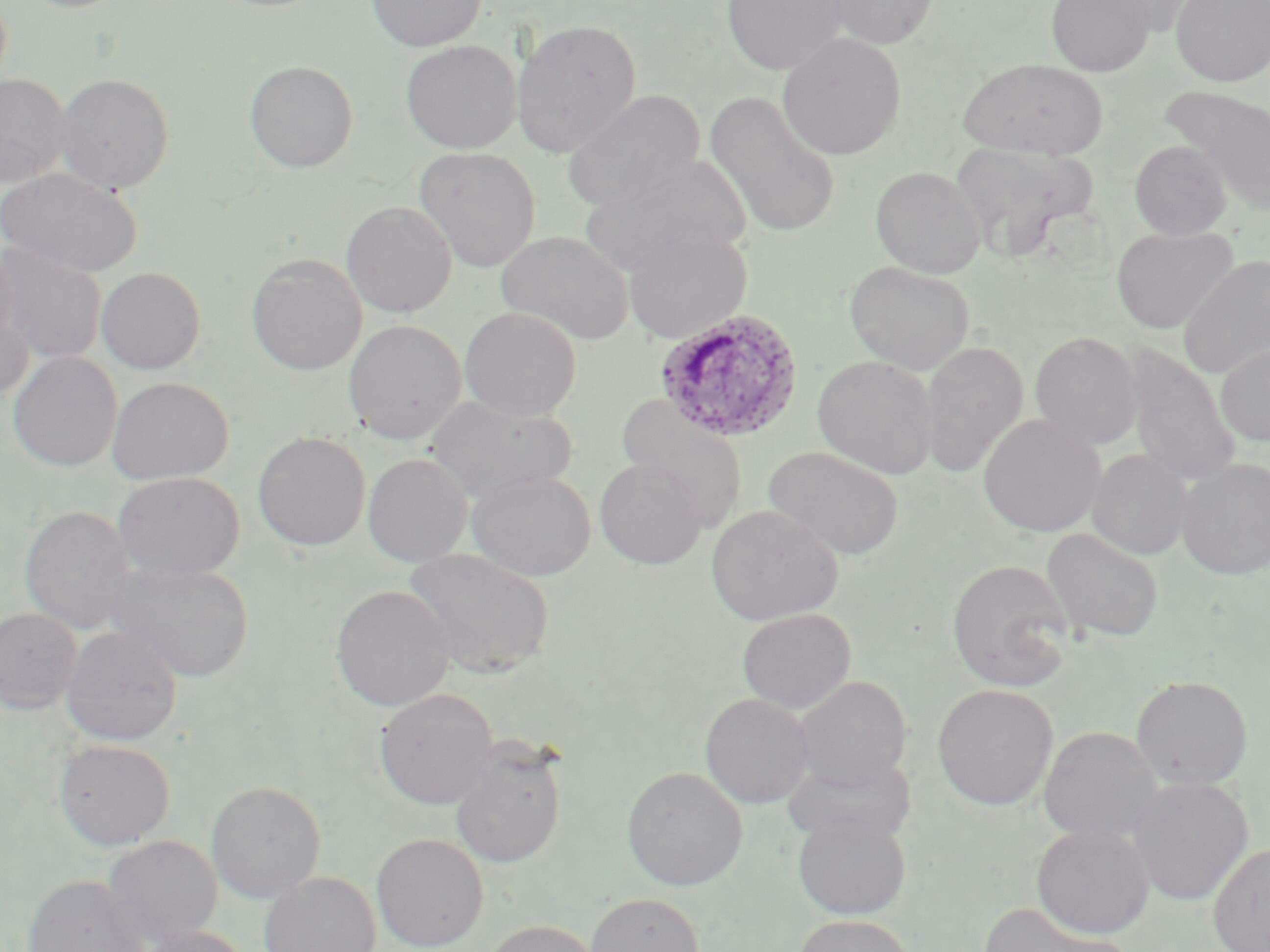
Summary:
  - Coordinate format: approximate bounding boxes as (x1,y1)-(x2,y2) corner pairs in pixels
  - Plasmodium ovale-infected red blood cell locations: (654,309)-(804,444)
  - Uninfected red blood cell locations: (366,0)-(486,52), (721,0)-(849,74), (822,0)-(939,50), (1046,0)-(1156,76), (1170,1)-(1270,87), (510,19)-(642,157), (776,33)-(907,161), (400,40)-(522,153), (959,57)-(1109,159), (244,60)-(358,172), (54,73)-(174,193), (0,74)-(71,188), (1162,86)-(1270,215), (562,89)-(706,212), (705,91)-(842,239), (1129,139)-(1232,239), (950,141)-(1096,261), (414,147)-(541,273), (580,155)-(752,276), (870,166)-(986,278), (0,167)-(142,276), (340,200)-(457,317), (622,224)-(752,344), (1111,226)-(1238,334), (495,230)-(635,344), (0,240)-(21,351), (1,243)-(107,365), (246,253)-(367,375), (1178,255)-(1270,378), (845,261)-(976,375), (96,266)-(206,373), (0,303)-(34,407), (459,307)-(582,421), (343,319)-(466,445), (1030,331)-(1143,448), (919,340)-(1029,479), (1215,342)-(1270,447), (1123,346)-(1241,482), (8,351)-(122,471), (812,355)-(940,479), (107,376)-(233,484), (425,394)-(576,503), (617,395)-(750,532), (978,413)-(1106,538), (252,431)-(371,551), (764,446)-(905,560), (1085,449)-(1195,560), (363,452)-(472,567), (595,457)-(709,569), (1175,458)-(1270,580), (465,468)-(596,582), (112,471)-(244,583), (706,504)-(843,626), (19,505)-(136,635), (1042,527)-(1165,643), (403,547)-(555,680), (946,558)-(1076,691), (103,561)-(255,682), (330,584)-(455,712), (0,607)-(82,713), (736,608)-(856,714), (61,625)-(182,745), (793,674)-(912,791), (1130,675)-(1254,791), (932,684)-(1059,810), (375,688)-(500,810), (699,692)-(815,809), (1038,726)-(1164,845), (449,738)-(567,868), (54,739)-(176,851), (783,753)-(917,845), (622,766)-(748,890), (1128,777)-(1254,905), (206,781)-(326,903), (792,813)-(912,920), (1031,822)-(1156,939), (371,832)-(488,952), (103,834)-(223,947), (1208,842)-(1270,951), (259,871)-(382,952), (22,874)-(151,952), (585,892)-(705,952), (978,901)-(1130,952), (793,914)-(915,952), (483,919)-(601,952), (135,924)-(253,952)
  - Slide-level diagnosis: Plasmodium ovale
  - Modality: light microscopy
  - Preparation: thin blood smear
  - Image size: 1270×952 pixels
  - Field of view: single
  - Magnification: 1000x
  - Stain: May-Grünwald-Giemsa